State which parasite is depicted.
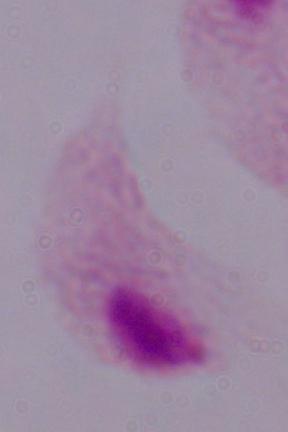
This is a trichomonad.

{
  "modality": "photomicrograph",
  "magnification": "1000x"
}